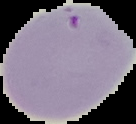
image_size: 136×124 pixels
preparation: thin blood film
image_type: cell region segmented out of the field of view; surrounding area masked to black
malaria_status: parasitized